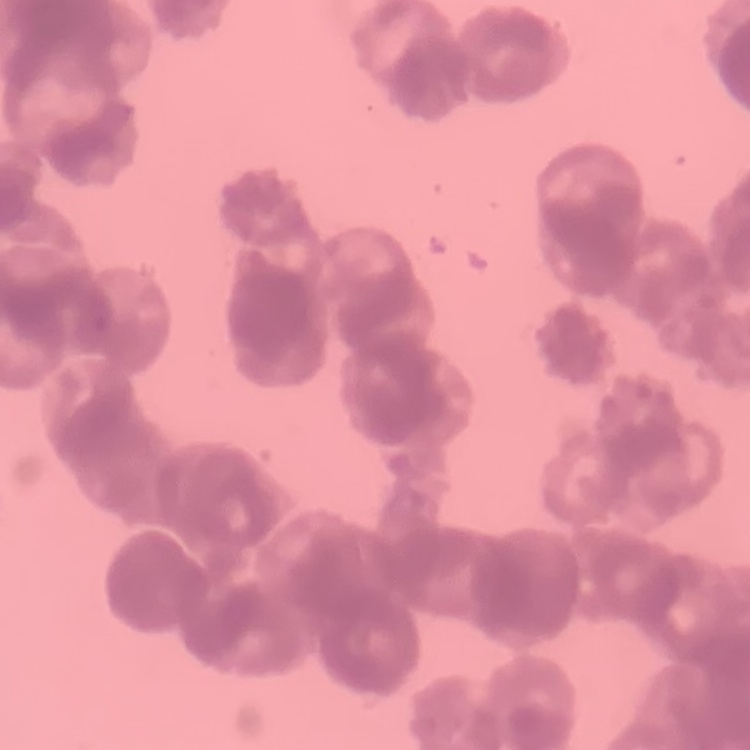

The erythrocytes exhibit rouleaux formation. Field's or Giemsa stain. Thin blood smear. Square crop of a larger photomicrograph.